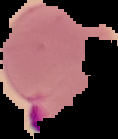
result: malaria parasites detected
image_type: cell region segmented out of the field of view; surrounding area masked to black
preparation: thin blood smear
image_size: 118×139 pixels